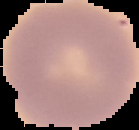
From a thin blood smear. Segmented cell region on a black background. Image is 139×130 pixels. Result: negative for Plasmodium parasites.